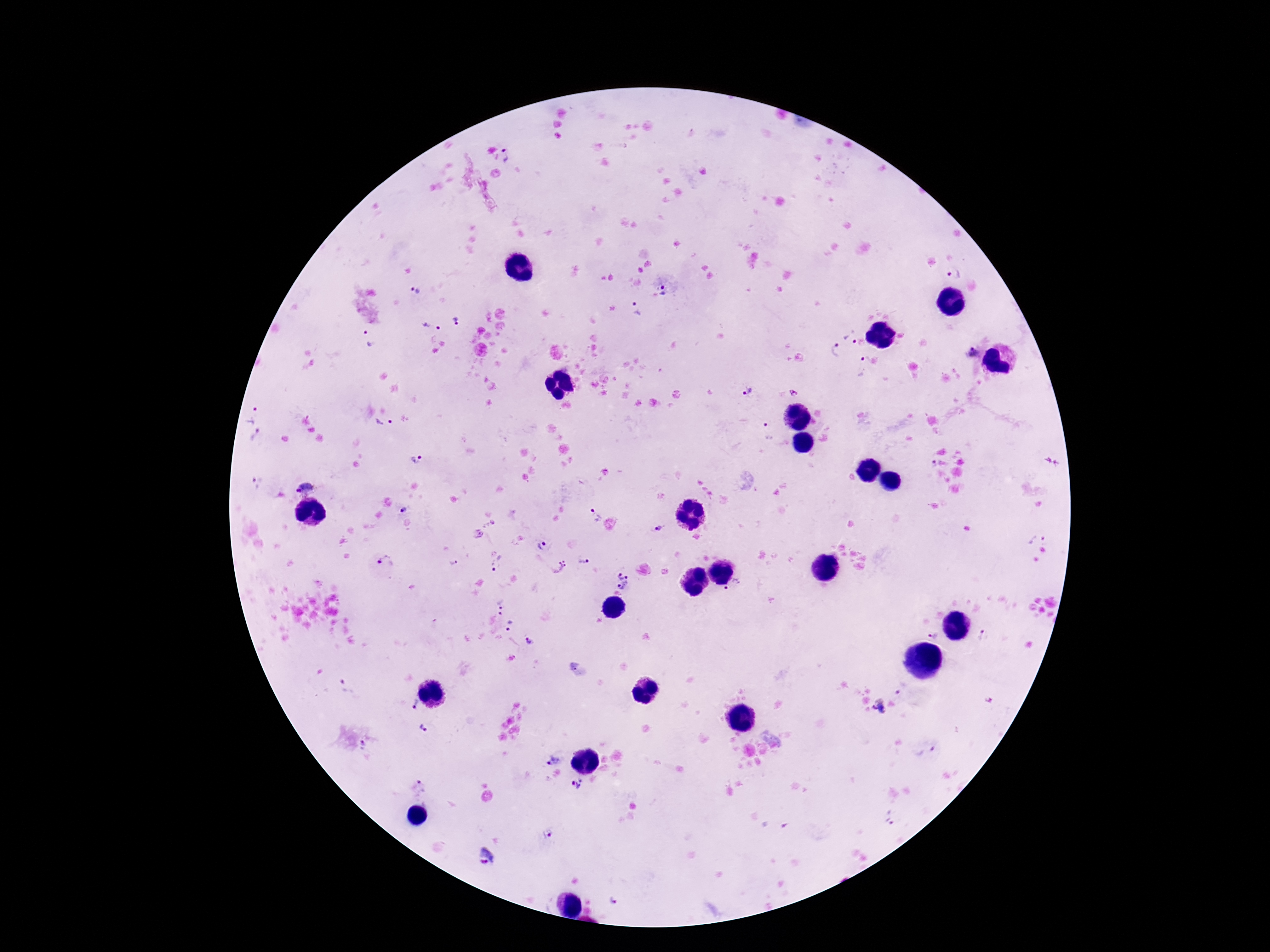
Approximate object centers, in pixels from the top-left corner. Plasmodium parasite locations: (x=508, y=156), (x=954, y=275), (x=664, y=291), (x=416, y=292), (x=635, y=309), (x=456, y=321), (x=433, y=327), (x=853, y=337), (x=369, y=338), (x=835, y=350), (x=971, y=353), (x=862, y=365), (x=747, y=391), (x=795, y=392), (x=252, y=413), (x=385, y=423), (x=767, y=432), (x=256, y=436), (x=416, y=460), (x=933, y=464), (x=258, y=481), (x=306, y=486), (x=403, y=510), (x=594, y=516), (x=657, y=530), (x=478, y=533), (x=1036, y=536), (x=543, y=546), (x=386, y=561), (x=583, y=561), (x=453, y=562), (x=497, y=565), (x=558, y=566), (x=623, y=582), (x=733, y=589), (x=501, y=602), (x=498, y=616), (x=510, y=625), (x=933, y=633), (x=982, y=633), (x=530, y=641), (x=902, y=688), (x=413, y=703), (x=878, y=708), (x=424, y=728), (x=365, y=745), (x=926, y=751), (x=554, y=760), (x=576, y=783), (x=420, y=790), (x=890, y=818), (x=548, y=834), (x=486, y=857), (x=615, y=897). Smartphone photograph taken through the microscope eyepiece. 100x magnification. Image is 1270×952 pixels. Thick blood film. Patient malaria status: positive. One field from this slide. Giemsa-stained preparation.